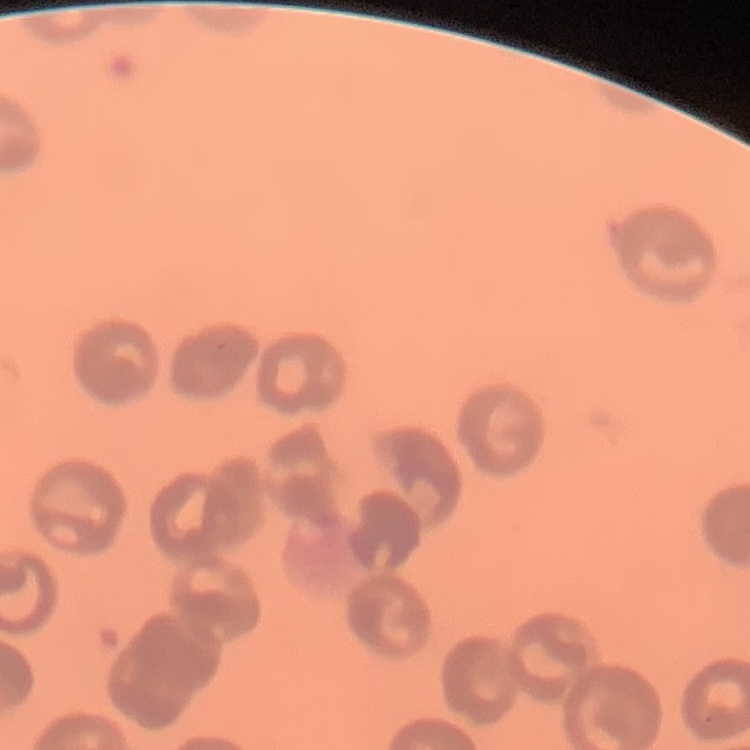
Summary:
  - Red blood cell morphology: no rouleaux formation
  - Preparation: thin peripheral smear
  - Stain: Field's or Giemsa
  - Image type: one tile cut from a larger photomicrograph